Locate every P. falciparum parasite and give its life-cycle stage, and locate every leukocyte and any debris.
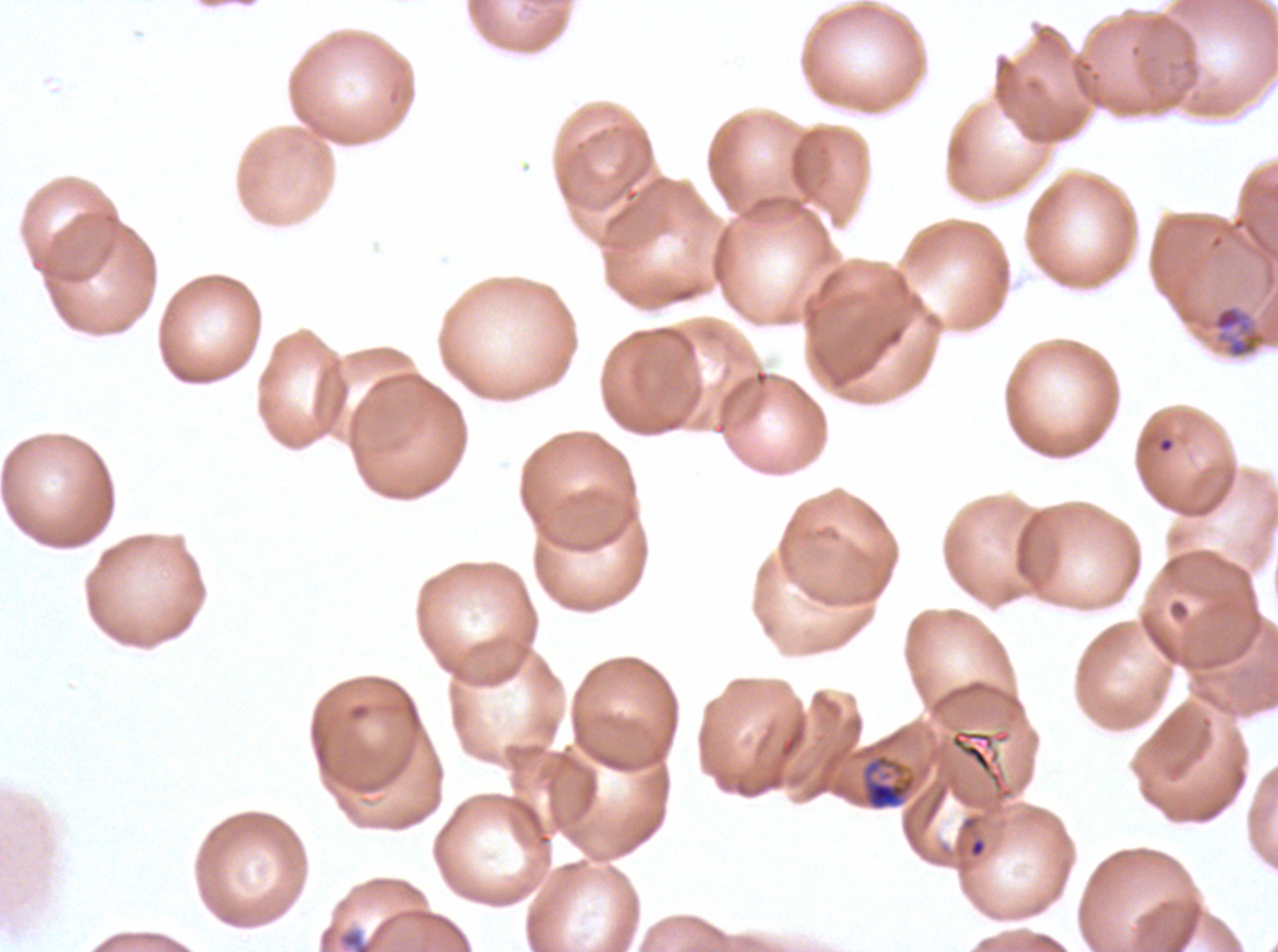
Approximate bounding rectangles given as corner coordinates in pixels from the top-left.
Mid trophozoites: (x1=1212, y1=305, x2=1265, y2=359), (x1=861, y1=752, x2=916, y2=812).
Debris: (x1=338, y1=928, x2=374, y2=951).
No rings, late-ring/early-trophozoite forms, late trophozoites, early schizonts, late schizonts, segmenters, gametocytes, or leukocytes observed.

{
  "specimen": "ex-vivo P. falciparum culture from a patient in The Gambia, grown for 24 to 48 hours",
  "field_of_view": "one sub-image of a larger composite",
  "preparation": "thin blood smear",
  "stain": "Giemsa",
  "image_size": "1278×952 pixels"
}